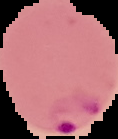
Summary:
  - Preparation: thin blood smear
  - Malaria status: parasitized
  - Image type: cell region segmented out of the field of view; surrounding area masked to black
  - Image size: 118×139 pixels